Point out leukocytes.
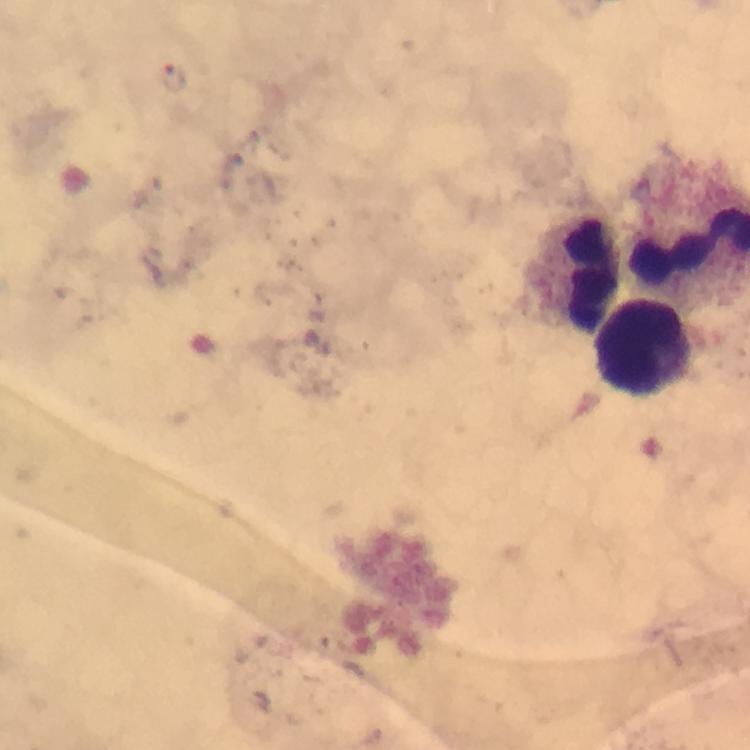

Approximate object centers, in pixels from the top-left corner.
Leukocytes: (x=594, y=276), (x=647, y=347).

Plasmodium parasite locations: (x=175, y=77). Thick blood film. At 100x magnification. From a diagnostic examination for malaria. Photographed through the microscope with a smartphone camera. A crop from one field of view. Immersion oil applied. Image is 750×750 pixels. Giemsa-stained preparation.